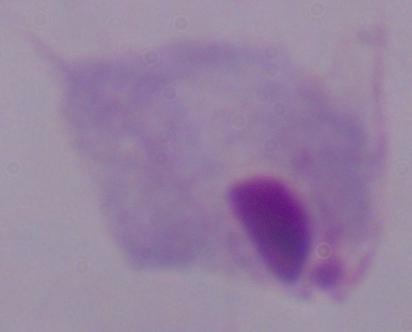
Summary:
  - Magnification: 1000x
  - Identification: trichomonad
  - Modality: micrograph